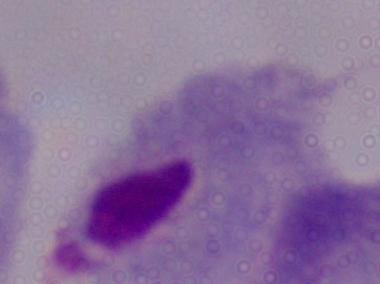
identification = trichomonad
magnification = 1000x
modality = micrograph